Describe the morphology of the erythrocytes.
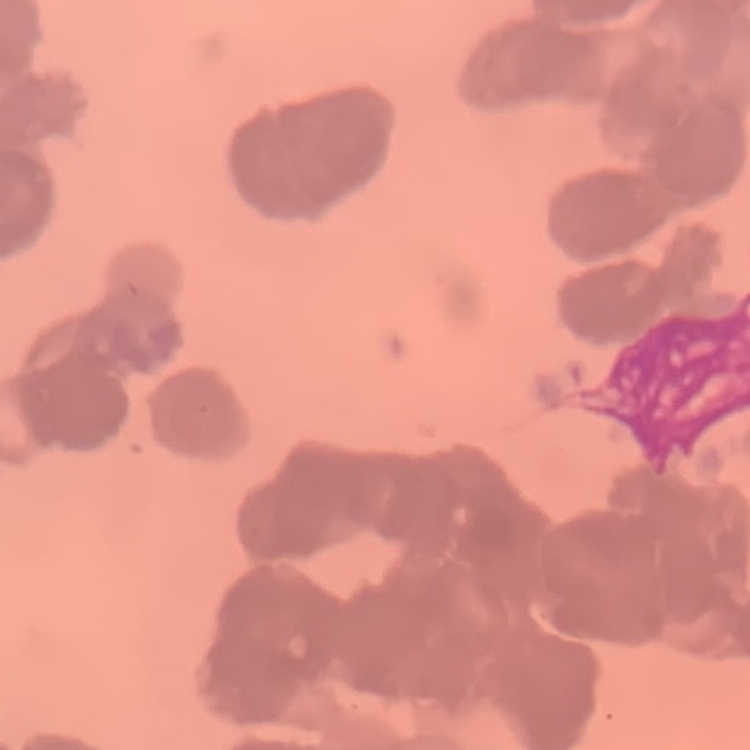

Rouleaux formation.

preparation: thin blood film
stain: Field's or Giemsa
image_type: square crop of a larger photomicrograph